Point out each Plasmodium parasite.
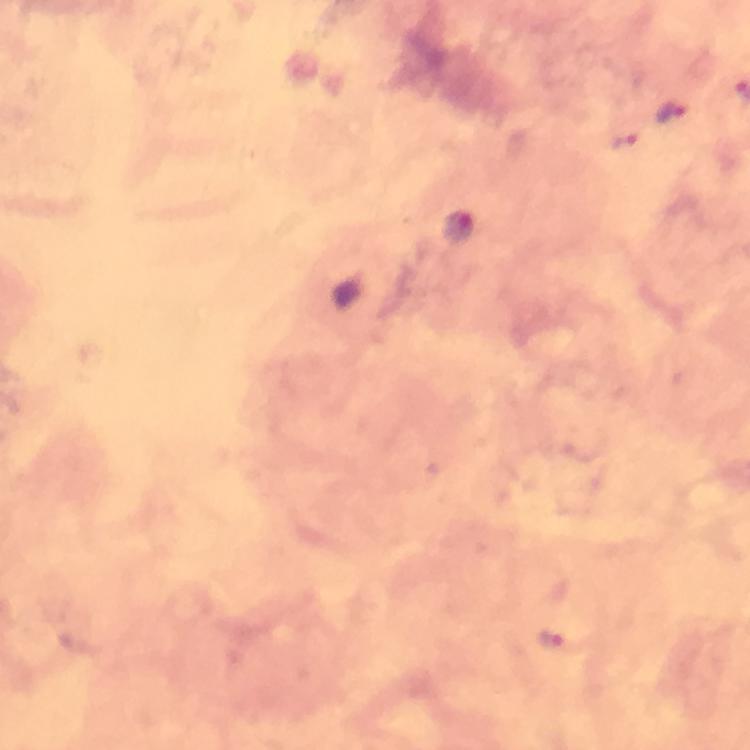

Approximate centers as {x, y} in pixels.
Plasmodium parasites: {671, 113}, {458, 226}, {551, 642}.

Image is 750×750 pixels. At 100x magnification. Photographed with a smartphone mounted on the microscope. Cropped region of a single field of view. Giemsa-stained preparation. Immersion oil applied. Thick blood smear. From a malaria diagnostic workup.